Name the cell type shown.
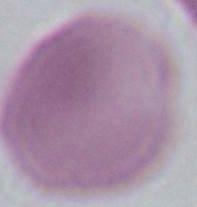
An erythrocyte.

Summary:
  - Magnification: 1000x
  - Modality: micrograph